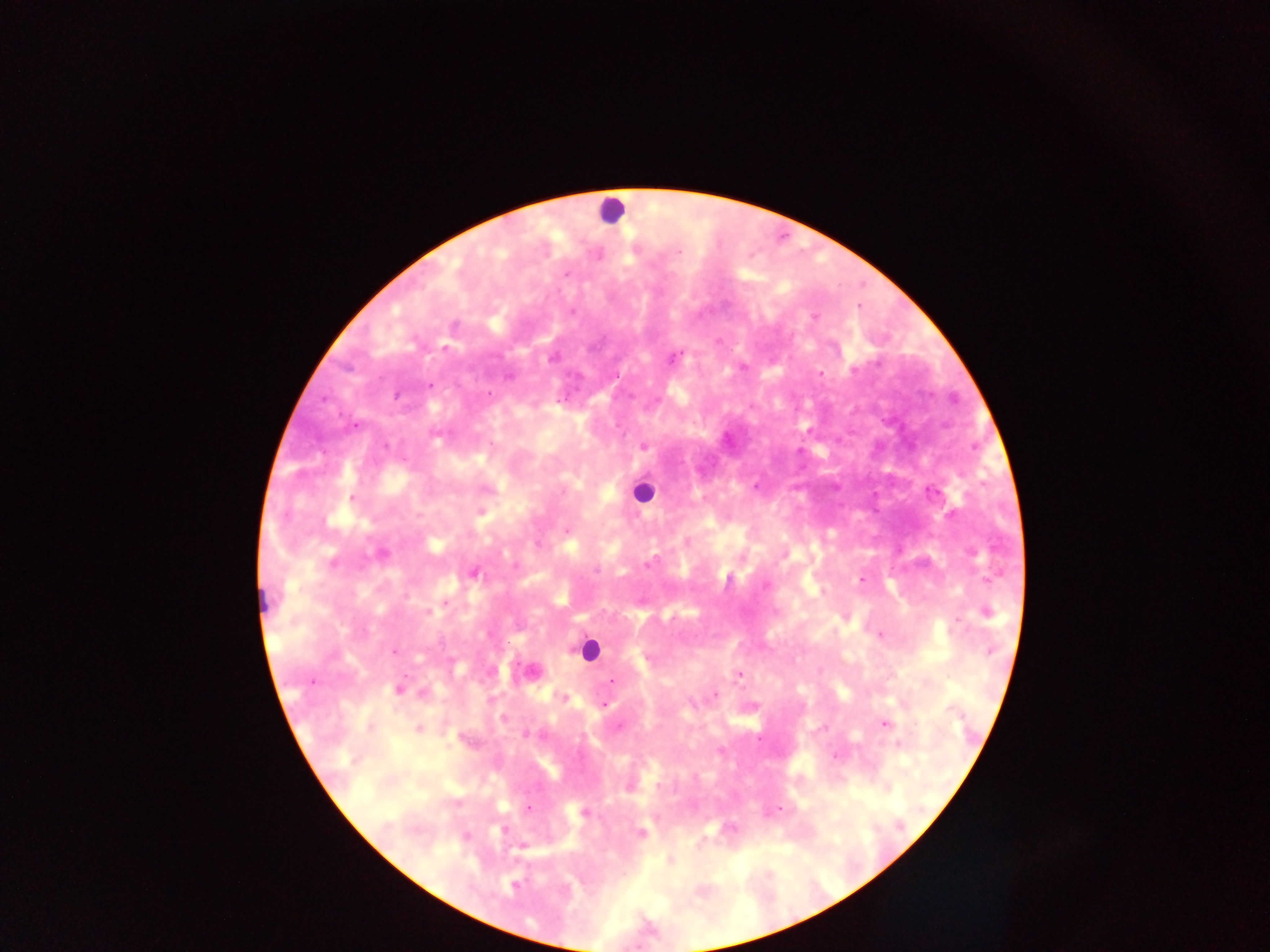
Approximate centers as [x, y] in pixels. Malaria parasite locations: [679, 252], [566, 275], [572, 311], [813, 317], [552, 358], [674, 358], [743, 366], [819, 374], [430, 386], [489, 394], [396, 396], [324, 398], [385, 446], [643, 446], [756, 486], [352, 499], [566, 530], [381, 553], [649, 562], [333, 563], [515, 566], [596, 570], [475, 573], [861, 579], [988, 579], [766, 586], [446, 603], [429, 612], [986, 612], [957, 621], [880, 635], [395, 650], [990, 650], [738, 675], [611, 680], [311, 682], [399, 690], [423, 693], [715, 695], [564, 698], [692, 703], [604, 705], [503, 719], [884, 723], [619, 727], [418, 729], [525, 735], [837, 755], [528, 808], [779, 809], [584, 812], [503, 830], [641, 832], [514, 886]. Leukocyte locations: [611, 211], [643, 492], [588, 650]. Image is 1270×952 pixels. One field of view. Thick blood smear. Photographed through a microscope with a mobile-phone camera. Collected in Ghana.